Name the blood parasite species.
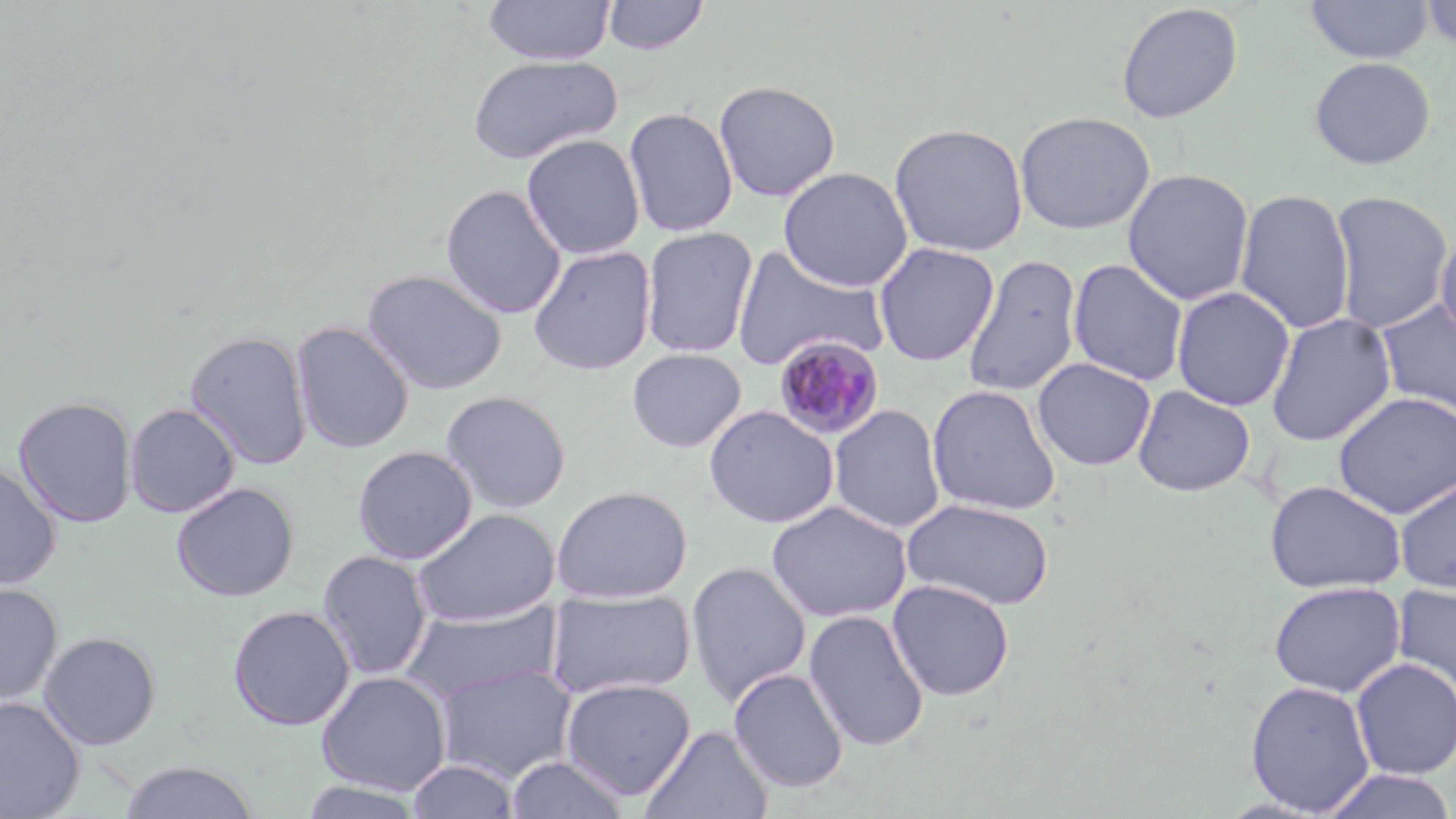
Plasmodium malariae.

Approximate bounding boxes as (x1,y1)-(x2,y2) corner pairs in pixels. Plasmodium malariae-infected red blood cell locations: (773,335)-(886,442). Uninfected red blood cell locations: (483,0)-(615,65), (601,0)-(710,55), (1305,1)-(1434,64), (1420,1)-(1456,50), (1116,3)-(1243,123), (465,54)-(623,165), (1309,56)-(1436,170), (714,79)-(841,201), (623,106)-(739,238), (1015,110)-(1156,235), (889,121)-(1029,257), (522,133)-(645,260), (778,166)-(913,292), (1122,168)-(1255,306), (440,184)-(567,319), (1234,188)-(1356,334), (1328,190)-(1454,334), (642,226)-(759,359), (1435,229)-(1456,347), (873,242)-(1000,366), (528,245)-(657,376), (731,246)-(891,372), (961,253)-(1083,399), (1067,258)-(1189,387), (362,269)-(507,395), (1171,286)-(1295,412), (1374,299)-(1456,418), (1266,313)-(1397,446), (291,321)-(414,454), (185,330)-(313,470), (627,348)-(746,452), (1032,357)-(1157,471), (926,383)-(1061,516), (1132,384)-(1256,497), (440,389)-(572,514), (1332,392)-(1456,519), (14,395)-(138,528), (124,402)-(240,518), (829,403)-(946,535), (703,404)-(839,528), (352,445)-(478,564), (0,461)-(61,590), (1394,476)-(1456,594), (1265,480)-(1406,594), (171,482)-(299,602), (551,485)-(693,602), (901,497)-(1055,611), (766,500)-(912,624), (412,508)-(560,626), (317,550)-(433,680), (686,560)-(811,708), (887,579)-(1015,701), (1268,580)-(1405,698), (1392,581)-(1456,700), (0,584)-(63,706), (544,587)-(697,700), (400,601)-(564,705), (228,604)-(355,730), (804,608)-(929,752), (39,631)-(162,750), (1350,658)-(1456,780), (434,662)-(577,782), (729,668)-(849,793), (315,670)-(452,795), (560,678)-(697,800), (1245,679)-(1376,816), (0,697)-(85,819), (642,724)-(774,819), (504,755)-(632,818), (118,760)-(260,818), (407,760)-(519,819), (1320,768)-(1456,819), (297,779)-(429,818). One field of a larger specimen. Image is 1456×819 pixels. Thin blood film. Optical microscopy. May-Grünwald-Giemsa-stained preparation. 1000x magnification.